Name the parasite shown.
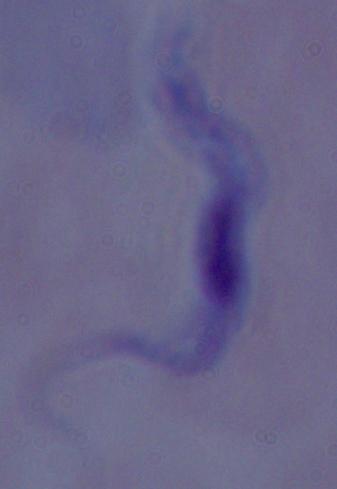

This is a trypanosome.

modality: photomicrograph
magnification: 1000x